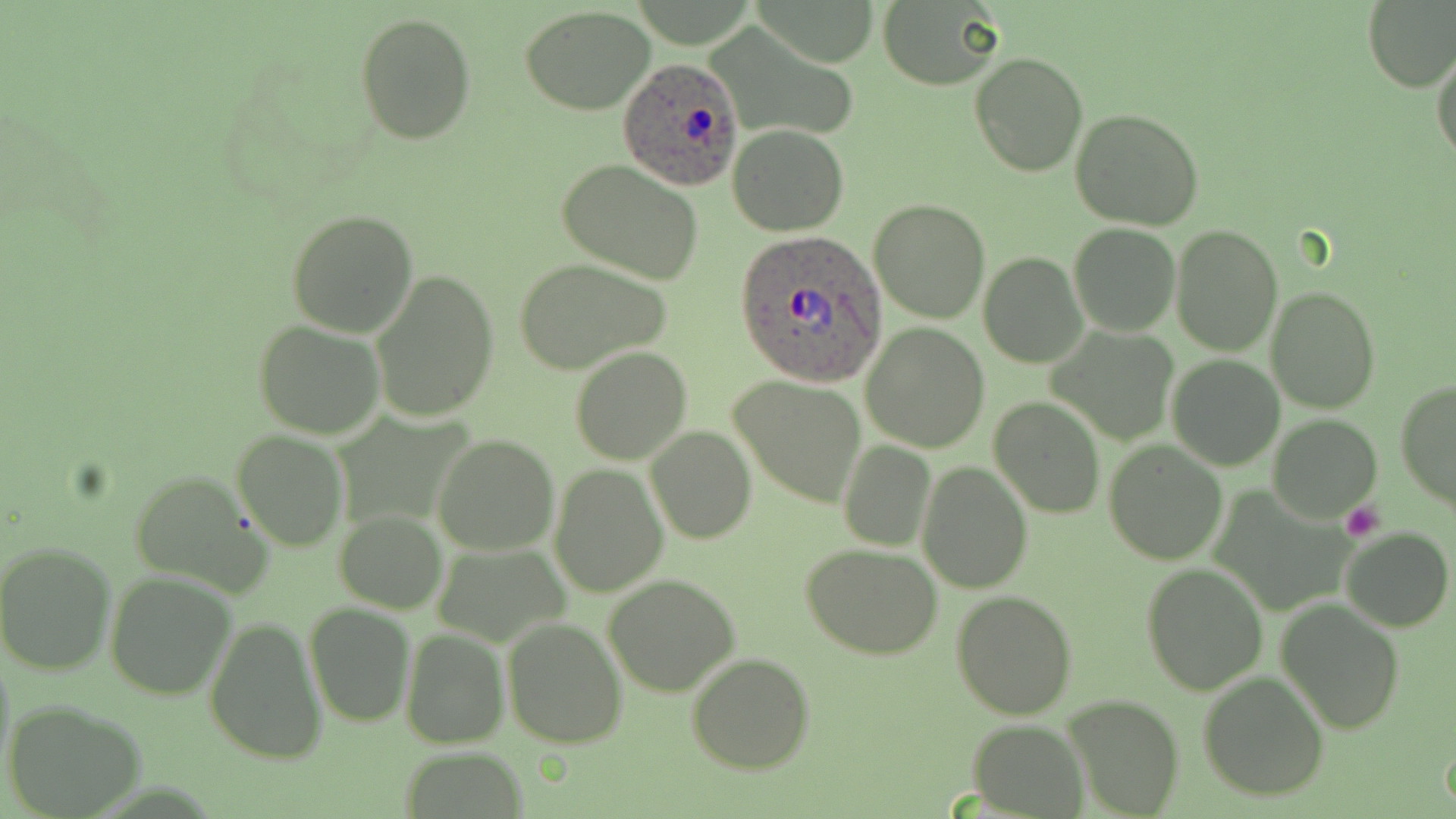
Summary:
  - Coordinate format: approximate bounding boxes as (x1,y1)-(x2,y2) corner pairs in pixels
  - Platelet locations: (1340,501)-(1385,542)
  - Plasmodium ovale-infected red blood cell locations: (620,58)-(742,189), (734,229)-(887,385)
  - Uninfected red blood cell locations: (877,0)-(1003,90), (1362,0)-(1456,92), (521,6)-(657,113), (354,14)-(476,144), (1432,46)-(1455,168), (970,51)-(1088,176), (1071,107)-(1205,229), (728,124)-(848,236), (556,158)-(705,284), (869,200)-(990,324), (287,209)-(418,336), (1067,223)-(1180,337), (1170,223)-(1283,355), (978,253)-(1085,368), (512,256)-(672,375), (368,270)-(497,423), (1266,286)-(1379,412), (252,320)-(385,439), (861,323)-(990,451), (1054,324)-(1177,443), (570,345)-(693,464), (1167,355)-(1285,470), (728,375)-(867,507), (1396,378)-(1456,515), (991,398)-(1104,517), (1267,415)-(1382,522), (644,426)-(757,546), (231,430)-(347,551), (432,434)-(560,556), (838,439)-(935,552), (1103,440)-(1228,564), (917,461)-(1032,592), (550,465)-(667,596), (128,469)-(270,593), (334,510)-(447,614), (1340,525)-(1453,633), (0,539)-(118,678), (431,541)-(570,648), (801,543)-(945,660), (1140,561)-(1269,696), (105,572)-(236,700), (603,573)-(741,696), (950,590)-(1077,720), (1275,597)-(1406,736), (303,601)-(416,728), (203,612)-(327,765), (504,618)-(628,747), (400,627)-(508,747), (687,653)-(816,774), (1196,670)-(1330,801), (1060,693)-(1185,819), (8,702)-(146,817), (968,719)-(1088,817)
  - Slide-level diagnosis: Plasmodium ovale
  - Modality: optical microscopy
  - Field of view: one of a larger specimen
  - Stain: May-Grünwald-Giemsa
  - Magnification: 1000x
  - Preparation: thin blood film
  - Image size: 1456×819 pixels